Name the parasite shown.
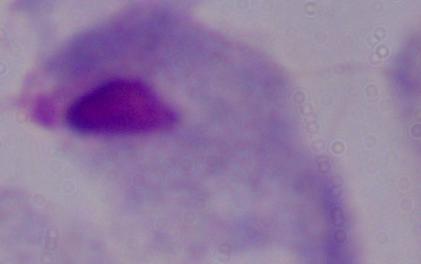

This is a trichomonad.

modality: micrograph
magnification: 1000x